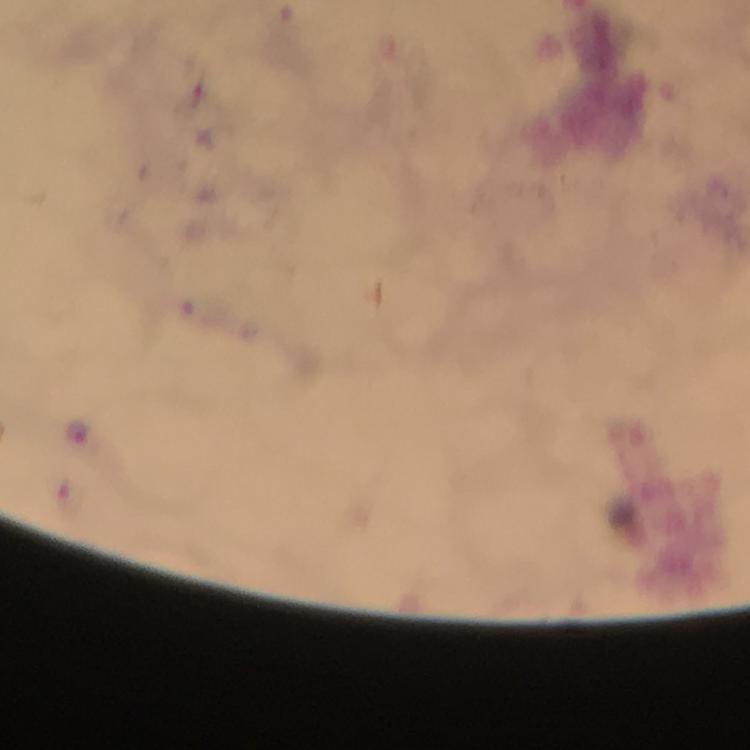
Approximate centers as (x, y) in pixels.
Summary:
  - Plasmodium parasite locations: (80, 435)
  - Cropped from: a single field of view
  - Image size: 750×750 pixels
  - Immersion oil: used
  - Stain: Giemsa
  - Context: from a diagnostic examination for malaria
  - Magnification: 100x
  - Preparation: thick blood film
  - Capture: smartphone photograph through a microscope